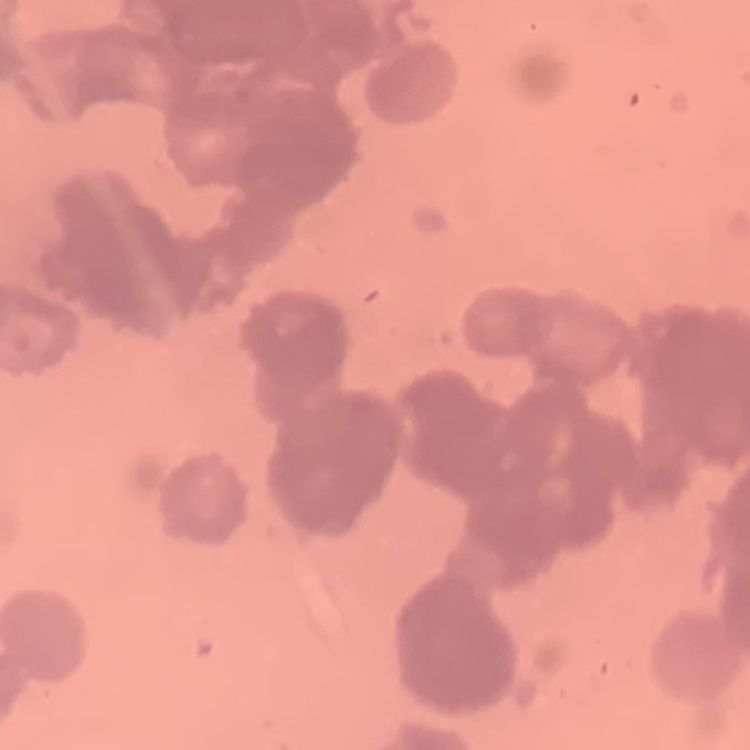

Summary:
  - Red blood cell morphology: rouleaux formation
  - Preparation: thin blood film
  - Stain: Field's or Giemsa
  - Image type: one tile cut from a larger photomicrograph